Name the parasite shown.
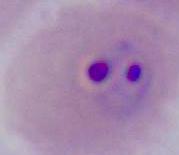
This is Plasmodium.

magnification = 400x or 1000x
modality = photomicrograph